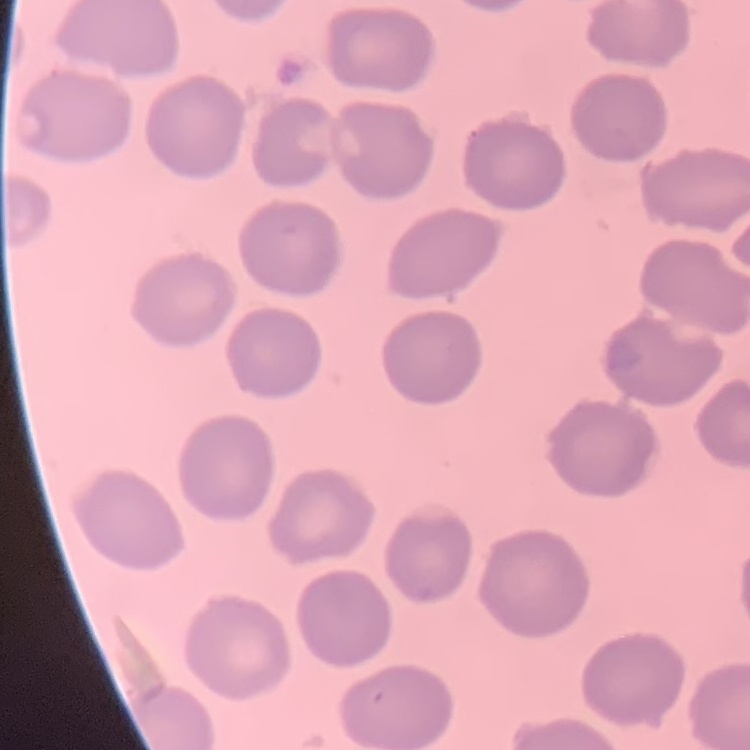 The erythrocytes exhibit no rouleaux formation. Stained with either Field's or Giemsa. Square crop of a larger photomicrograph. Thin peripheral smear.